Point out each leukocyte.
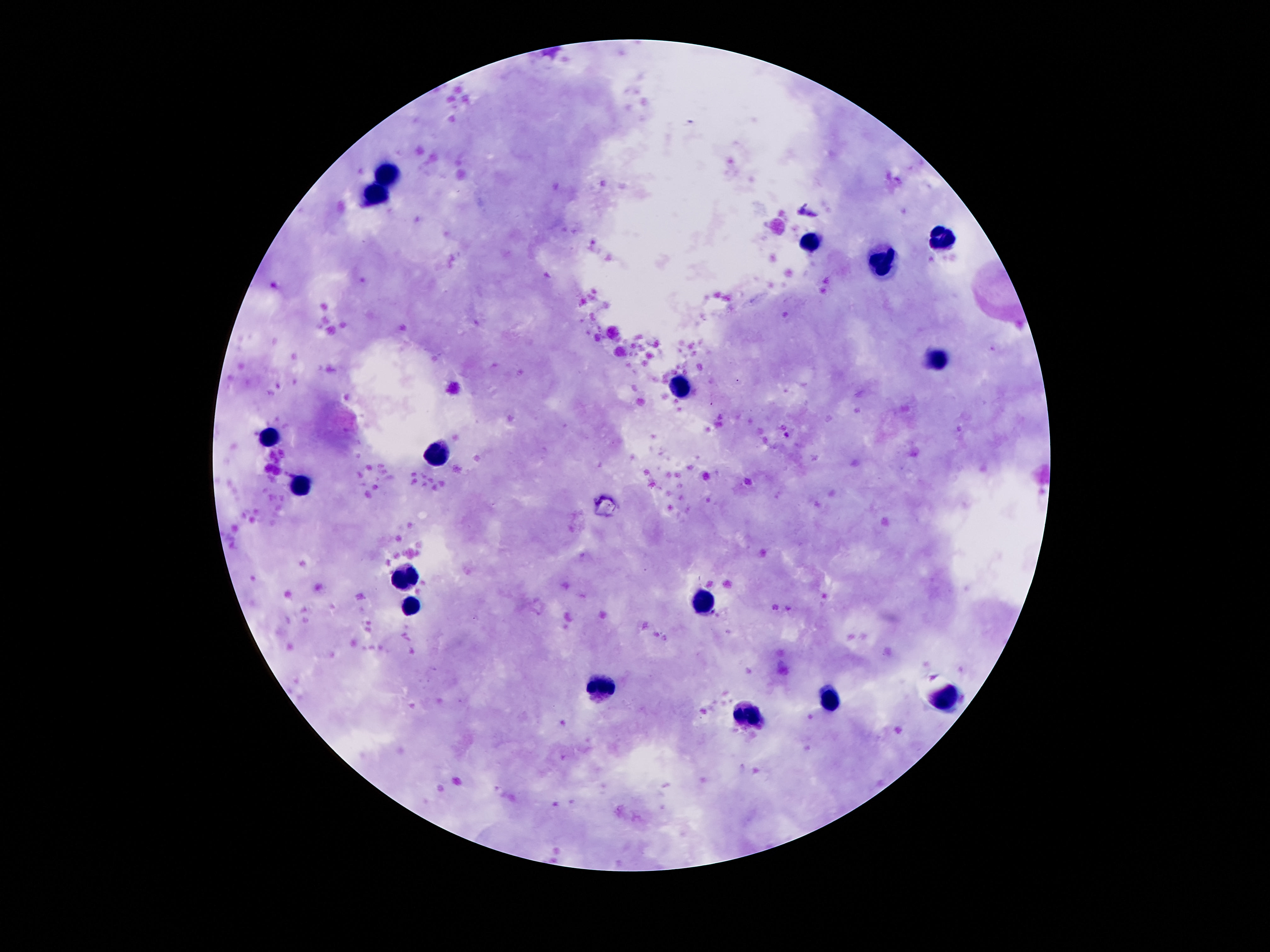

Approximate centers as {x, y} in pixels.
Leukocytes: {386, 174}, {375, 193}, {944, 238}, {808, 243}, {882, 266}, {938, 358}, {679, 385}, {269, 436}, {438, 452}, {300, 485}, {407, 572}, {700, 600}, {410, 608}, {601, 688}, {948, 695}, {832, 699}, {752, 717}.

Single field of view. Photographed through the microscope eyepiece with a smartphone camera. Image is 1270×952 pixels. Thick blood film. Patient malaria status: not infected. Giemsa-stained preparation. 100x magnification.